Classify this cell by malaria status.
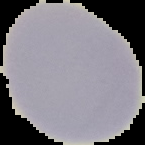
It is uninfected.

Cell region segmented out of the field of view; the surrounding area is masked to black. From a thin blood film. Image is 145×145 pixels.